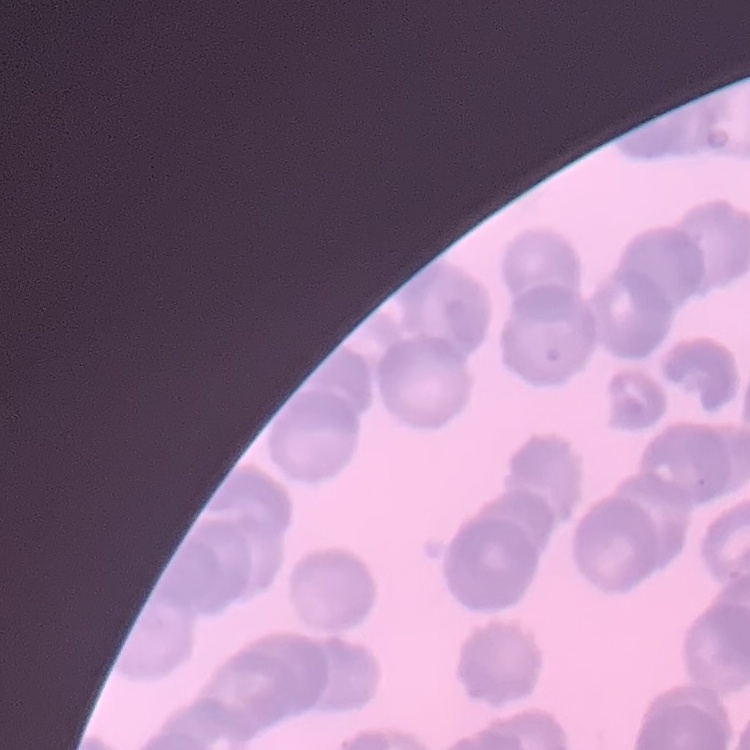
Summary:
  - Erythrocyte morphology: rouleaux formation
  - Preparation: thin blood film
  - Image type: square crop of a larger photomicrograph
  - Stain: Field's or Giemsa